Comment on the morphology of the erythrocytes.
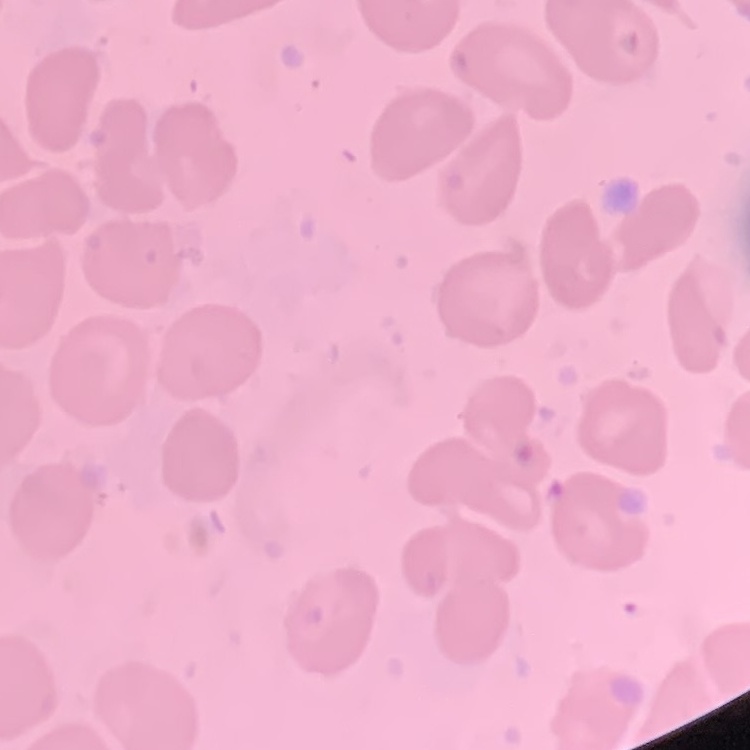

They show no rouleaux formation.

preparation: thin blood smear
image_type: one tile cut from a larger photomicrograph
stain: Field's or Giemsa